Name the blood parasite species.
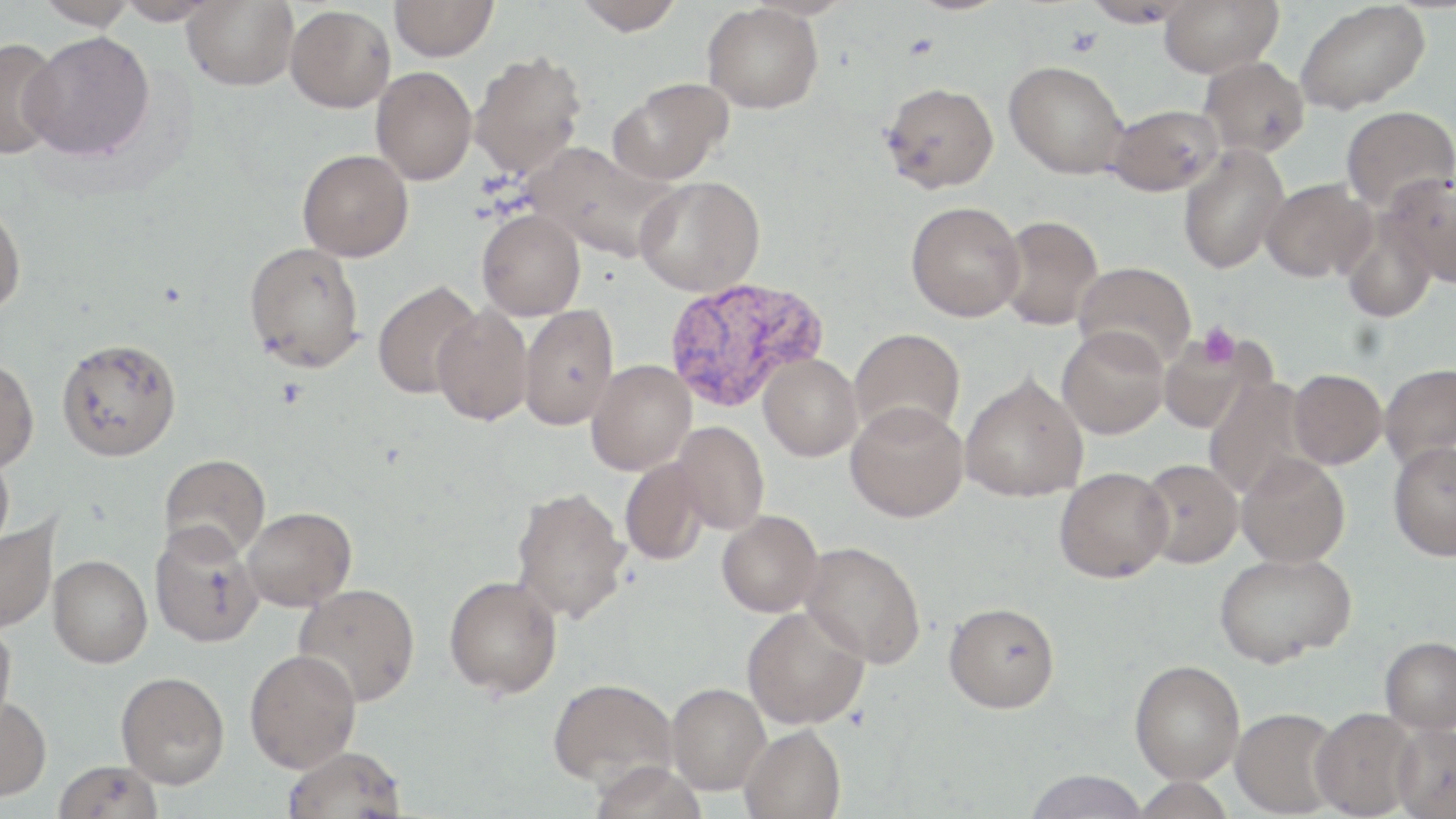
Plasmodium vivax.

Summary:
  - Coordinate format: approximate bounding boxes as [x1, y1, x2, y2] in pixels
  - Plasmodium vivax-infected red blood cell locations: [663, 277, 829, 413]
  - Uninfected red blood cell locations: [37, 0, 137, 30], [115, 0, 221, 25], [182, 0, 298, 90], [390, 0, 498, 61], [572, 0, 684, 35], [1158, 0, 1283, 77], [1295, 1, 1430, 115], [703, 3, 823, 113], [285, 5, 396, 112], [22, 31, 155, 160], [0, 37, 64, 159], [469, 51, 587, 180], [1199, 56, 1310, 158], [1005, 60, 1128, 178], [371, 66, 477, 185], [609, 78, 731, 184], [881, 82, 999, 193], [1106, 104, 1224, 196], [1340, 105, 1455, 212], [526, 142, 670, 259], [1178, 144, 1289, 274], [297, 149, 413, 261], [1380, 173, 1456, 287], [634, 176, 764, 296], [1261, 178, 1375, 282], [906, 201, 1025, 321], [0, 203, 26, 315], [477, 209, 585, 320], [997, 214, 1103, 330], [1341, 214, 1438, 324], [243, 242, 365, 372], [1074, 261, 1196, 370], [372, 281, 482, 399], [432, 304, 533, 426], [519, 304, 619, 430], [1057, 325, 1169, 439], [849, 328, 965, 440], [1159, 330, 1270, 434], [56, 336, 182, 461], [759, 354, 862, 461], [0, 357, 39, 473], [586, 360, 696, 475], [1379, 364, 1456, 470], [1288, 369, 1387, 469], [960, 373, 1088, 502], [1204, 376, 1316, 501], [845, 400, 969, 522], [672, 421, 769, 534], [1388, 441, 1456, 560], [0, 447, 15, 553], [159, 453, 271, 562], [1236, 453, 1350, 567], [1137, 458, 1243, 569], [620, 459, 707, 566], [1054, 466, 1174, 582], [511, 486, 630, 623], [243, 506, 356, 611], [716, 510, 822, 617], [0, 515, 60, 634], [149, 522, 264, 648], [799, 541, 925, 668], [1213, 551, 1355, 667], [48, 555, 152, 668], [444, 575, 562, 698], [294, 583, 420, 706], [944, 602, 1060, 713], [741, 606, 870, 730], [0, 617, 16, 733], [1380, 636, 1456, 734], [244, 649, 362, 772], [1129, 659, 1245, 784], [116, 671, 230, 789], [548, 677, 679, 787], [667, 683, 770, 795], [0, 696, 51, 801], [1230, 707, 1342, 817], [1310, 708, 1420, 818], [1391, 721, 1456, 819], [740, 724, 846, 819], [282, 746, 407, 819], [53, 759, 164, 819], [1022, 769, 1152, 818]
  - Platelet locations: [1197, 321, 1240, 369]
  - Magnification: 1000x
  - Modality: light microscopy
  - Field of view: single
  - Stain: May-Grünwald-Giemsa
  - Image size: 1456×819 pixels
  - Preparation: thin blood smear